Outline each blood parasite and name the species.
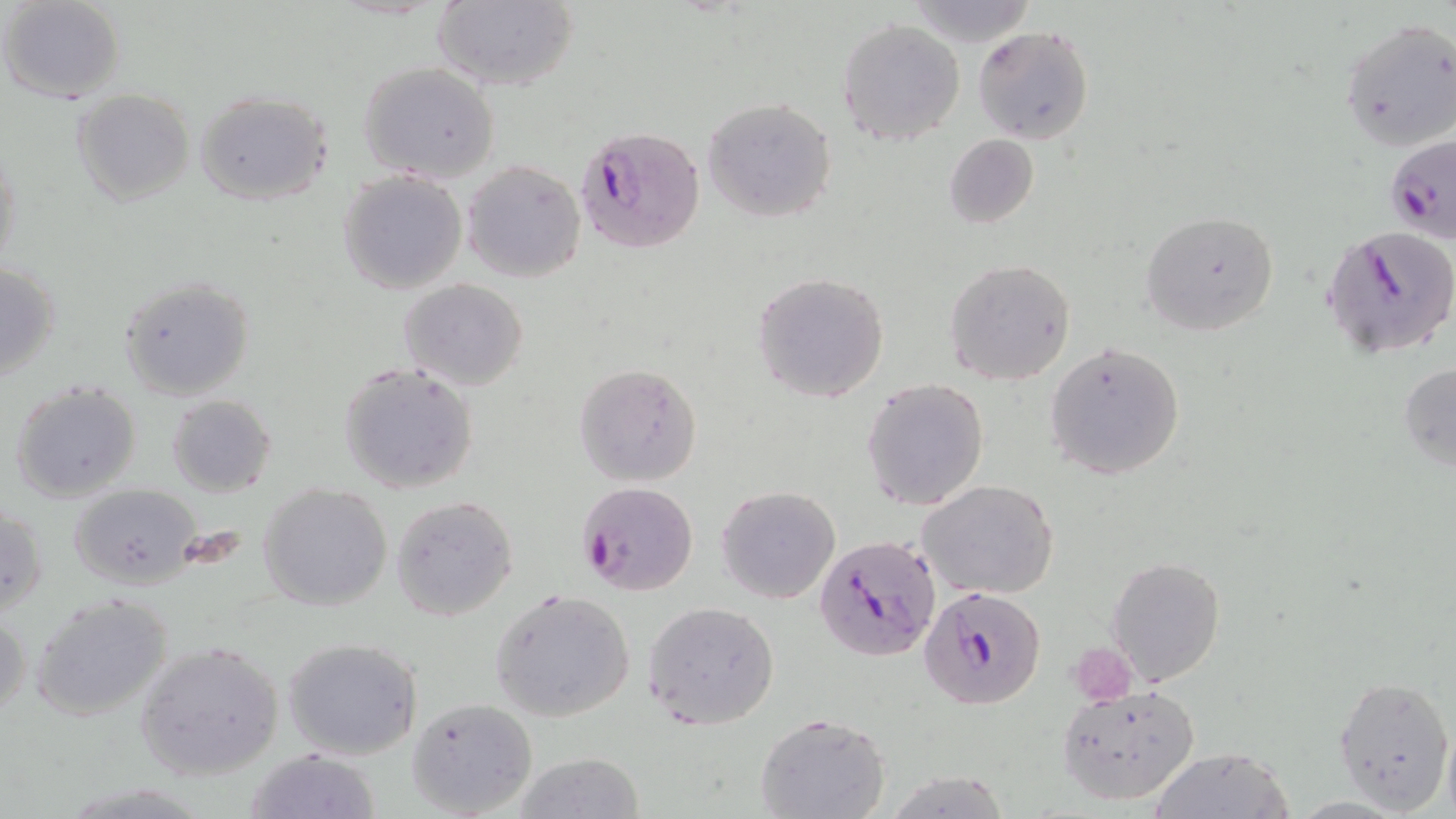
Approximate bounding boxes as named x1/y1/x2/y2 corners in pixels.
Plasmodium falciparum-infected red blood cells: (x1=579, y1=125, x2=707, y2=255), (x1=1382, y1=134, x2=1455, y2=244), (x1=1322, y1=226, x2=1456, y2=358), (x1=578, y1=480, x2=698, y2=595), (x1=814, y1=534, x2=941, y2=664), (x1=919, y1=585, x2=1047, y2=709).
No Plasmodium ovale, Plasmodium malariae, Plasmodium vivax, Babesia divergens, or Trypanosoma brucei observed.

Summary:
  - Uninfected red blood cell locations: (x1=0, y1=0, x2=126, y2=103), (x1=430, y1=0, x2=579, y2=93), (x1=904, y1=0, x2=1039, y2=48), (x1=837, y1=18, x2=966, y2=146), (x1=1341, y1=19, x2=1456, y2=153), (x1=974, y1=25, x2=1095, y2=145), (x1=358, y1=62, x2=499, y2=183), (x1=72, y1=89, x2=195, y2=206), (x1=195, y1=90, x2=334, y2=205), (x1=702, y1=95, x2=839, y2=224), (x1=944, y1=133, x2=1039, y2=227), (x1=1, y1=141, x2=22, y2=278), (x1=461, y1=161, x2=587, y2=282), (x1=338, y1=170, x2=468, y2=295), (x1=1140, y1=209, x2=1278, y2=336), (x1=944, y1=259, x2=1077, y2=385), (x1=1, y1=260, x2=63, y2=385), (x1=752, y1=272, x2=889, y2=402), (x1=118, y1=276, x2=257, y2=401), (x1=398, y1=277, x2=528, y2=390), (x1=1045, y1=341, x2=1186, y2=480), (x1=337, y1=362, x2=481, y2=497), (x1=575, y1=362, x2=701, y2=486), (x1=1398, y1=363, x2=1456, y2=471), (x1=8, y1=379, x2=142, y2=503), (x1=862, y1=379, x2=989, y2=509), (x1=167, y1=395, x2=277, y2=496), (x1=919, y1=479, x2=1061, y2=601), (x1=259, y1=482, x2=393, y2=611), (x1=66, y1=483, x2=203, y2=589), (x1=717, y1=486, x2=839, y2=605), (x1=390, y1=494, x2=519, y2=619), (x1=1, y1=503, x2=46, y2=618), (x1=1107, y1=556, x2=1226, y2=688), (x1=491, y1=588, x2=635, y2=722), (x1=29, y1=594, x2=175, y2=723), (x1=643, y1=600, x2=780, y2=729), (x1=0, y1=606, x2=30, y2=724), (x1=282, y1=636, x2=422, y2=759), (x1=135, y1=640, x2=284, y2=779), (x1=1333, y1=674, x2=1454, y2=812), (x1=1058, y1=683, x2=1200, y2=806), (x1=407, y1=697, x2=539, y2=817), (x1=756, y1=712, x2=890, y2=819), (x1=1441, y1=719, x2=1456, y2=819), (x1=1149, y1=747, x2=1293, y2=819), (x1=244, y1=748, x2=383, y2=819), (x1=511, y1=752, x2=645, y2=818)
  - Slide-level diagnosis: Plasmodium falciparum
  - Modality: light microscopy
  - Stain: May-Grünwald-Giemsa
  - Image size: 1456×819 pixels
  - Magnification: 1000x
  - Field of view: one of a larger specimen
  - Preparation: thin blood film